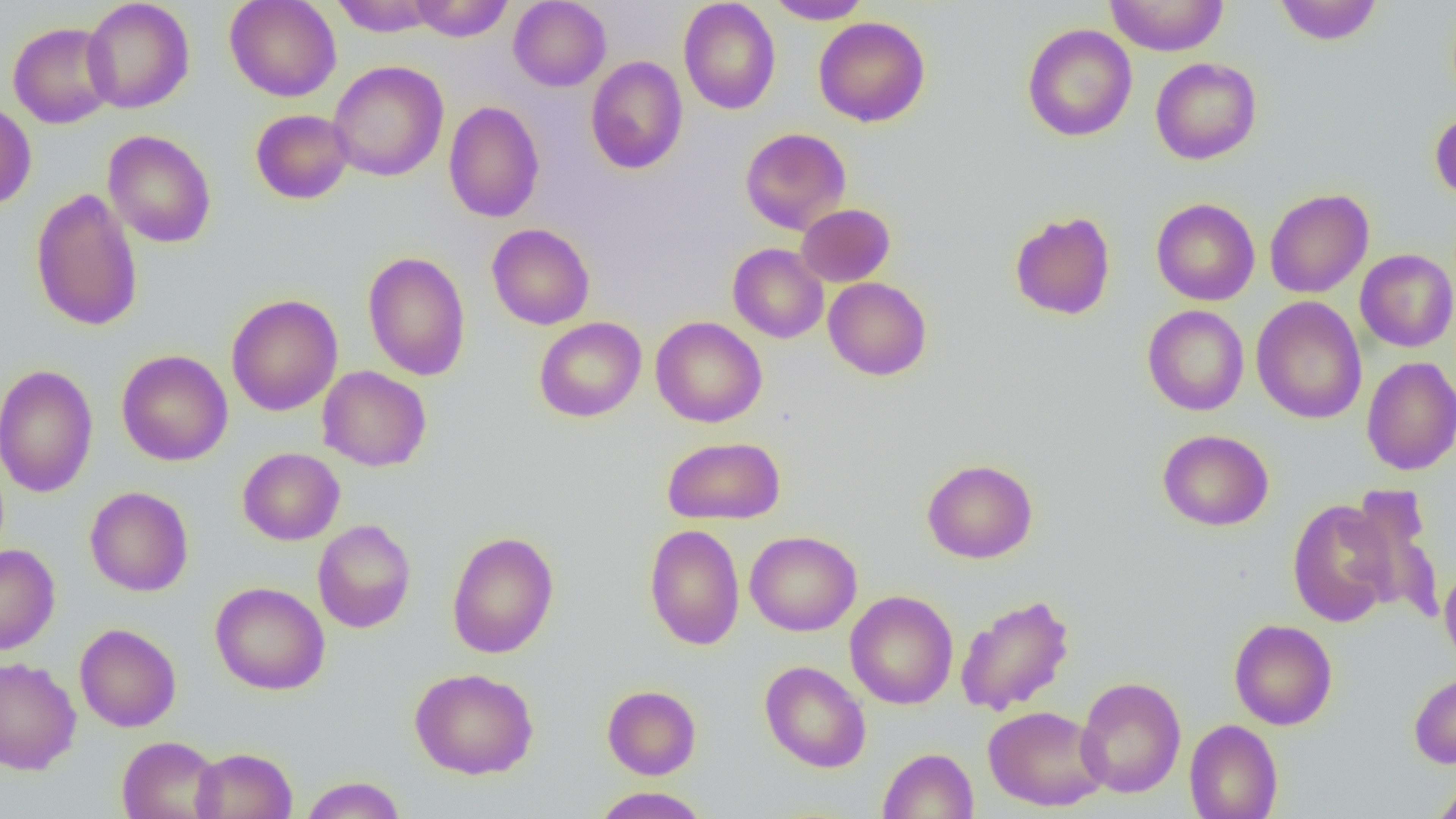

slide-level diagnosis = no evidence of blood parasites
uninfected red blood cell locations = approximate bounding boxes as named x1/y1/x2/y2 corners in pixels: (x1=81, y1=0, x2=195, y2=113), (x1=224, y1=0, x2=342, y2=101), (x1=330, y1=0, x2=440, y2=36), (x1=409, y1=0, x2=514, y2=41), (x1=508, y1=0, x2=611, y2=91), (x1=679, y1=0, x2=781, y2=115), (x1=765, y1=0, x2=871, y2=24), (x1=1105, y1=0, x2=1228, y2=56), (x1=1274, y1=1, x2=1382, y2=45), (x1=813, y1=17, x2=930, y2=127), (x1=8, y1=21, x2=118, y2=128), (x1=1022, y1=23, x2=1137, y2=142), (x1=586, y1=56, x2=688, y2=174), (x1=1150, y1=57, x2=1262, y2=164), (x1=328, y1=60, x2=449, y2=182), (x1=0, y1=101, x2=37, y2=210), (x1=443, y1=101, x2=544, y2=222), (x1=1430, y1=108, x2=1456, y2=204), (x1=250, y1=109, x2=354, y2=204), (x1=740, y1=127, x2=851, y2=234), (x1=102, y1=130, x2=217, y2=248), (x1=30, y1=187, x2=144, y2=332), (x1=1264, y1=188, x2=1373, y2=298), (x1=1151, y1=198, x2=1260, y2=306), (x1=796, y1=203, x2=895, y2=287), (x1=1009, y1=211, x2=1116, y2=320), (x1=487, y1=223, x2=595, y2=330), (x1=728, y1=243, x2=828, y2=343), (x1=1355, y1=249, x2=1456, y2=352), (x1=362, y1=251, x2=471, y2=381), (x1=823, y1=277, x2=932, y2=381), (x1=226, y1=294, x2=343, y2=416), (x1=1251, y1=296, x2=1366, y2=424), (x1=1142, y1=305, x2=1249, y2=416), (x1=650, y1=316, x2=767, y2=427), (x1=534, y1=317, x2=646, y2=422), (x1=117, y1=350, x2=232, y2=466), (x1=1361, y1=356, x2=1456, y2=475), (x1=0, y1=364, x2=99, y2=498), (x1=317, y1=365, x2=432, y2=472), (x1=1157, y1=429, x2=1274, y2=531), (x1=661, y1=436, x2=786, y2=525), (x1=237, y1=447, x2=344, y2=545), (x1=922, y1=459, x2=1037, y2=563), (x1=1343, y1=484, x2=1444, y2=621), (x1=85, y1=486, x2=193, y2=596), (x1=1287, y1=498, x2=1399, y2=627), (x1=312, y1=519, x2=416, y2=633), (x1=644, y1=523, x2=745, y2=650), (x1=446, y1=530, x2=559, y2=659), (x1=745, y1=530, x2=862, y2=636), (x1=0, y1=544, x2=60, y2=655), (x1=1440, y1=564, x2=1456, y2=669), (x1=210, y1=581, x2=330, y2=695), (x1=844, y1=590, x2=958, y2=709), (x1=955, y1=594, x2=1075, y2=716), (x1=1228, y1=619, x2=1338, y2=730), (x1=74, y1=623, x2=181, y2=732), (x1=0, y1=656, x2=81, y2=775), (x1=760, y1=661, x2=871, y2=773), (x1=409, y1=667, x2=539, y2=780), (x1=1409, y1=671, x2=1456, y2=768), (x1=1075, y1=676, x2=1186, y2=798), (x1=602, y1=685, x2=702, y2=779), (x1=983, y1=705, x2=1108, y2=811), (x1=1184, y1=719, x2=1283, y2=819), (x1=117, y1=735, x2=223, y2=819), (x1=190, y1=746, x2=297, y2=819), (x1=878, y1=748, x2=979, y2=818), (x1=300, y1=775, x2=407, y2=818), (x1=1430, y1=777, x2=1456, y2=819), (x1=592, y1=786, x2=709, y2=818)
modality = optical microscopy
image size = 1456×819 pixels
field of view = one of a larger specimen
preparation = thin blood smear
magnification = 1000x